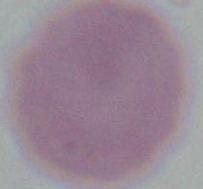

{
  "modality": "photomicrograph",
  "identification": "erythrocyte",
  "magnification": "1000x"
}